Comment on the morphology of the red blood cells.
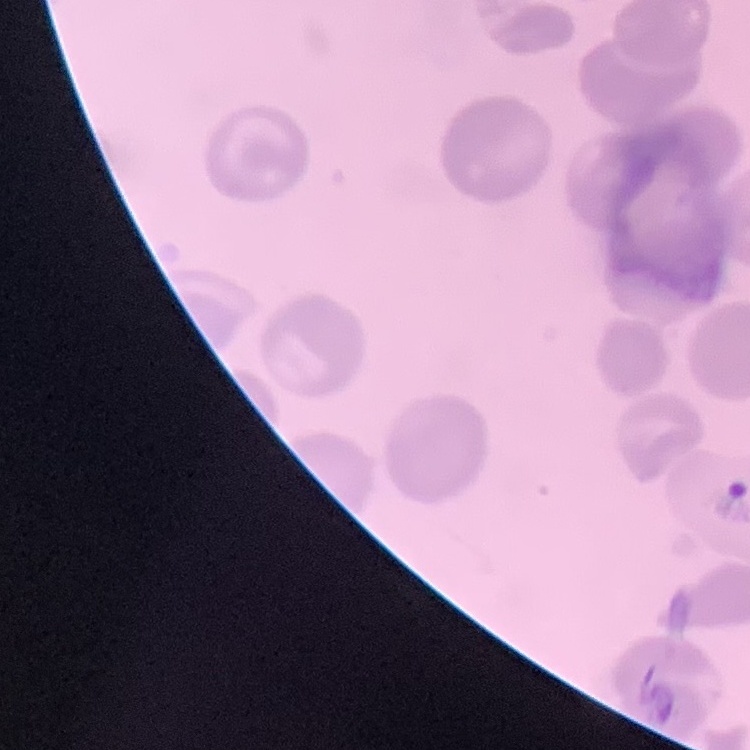

They show no rouleaux formation.

Summary:
  - Stain: Field's or Giemsa
  - Image type: square crop of a larger photomicrograph
  - Preparation: thin blood film